Report the malaria status of this cell.
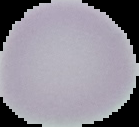

Uninfected.

The area outside the segmented cell region is set to black. Image is 139×127 pixels. From a thin blood film.